Classify this cell by malaria status.
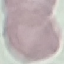

Uninfected.

Photographed with a smartphone camera at the microscope eyepiece. Thin blood film. Giemsa stain. Automatically extracted cell patch, resized to 64 × 64 pixels.